Report the malaria status.
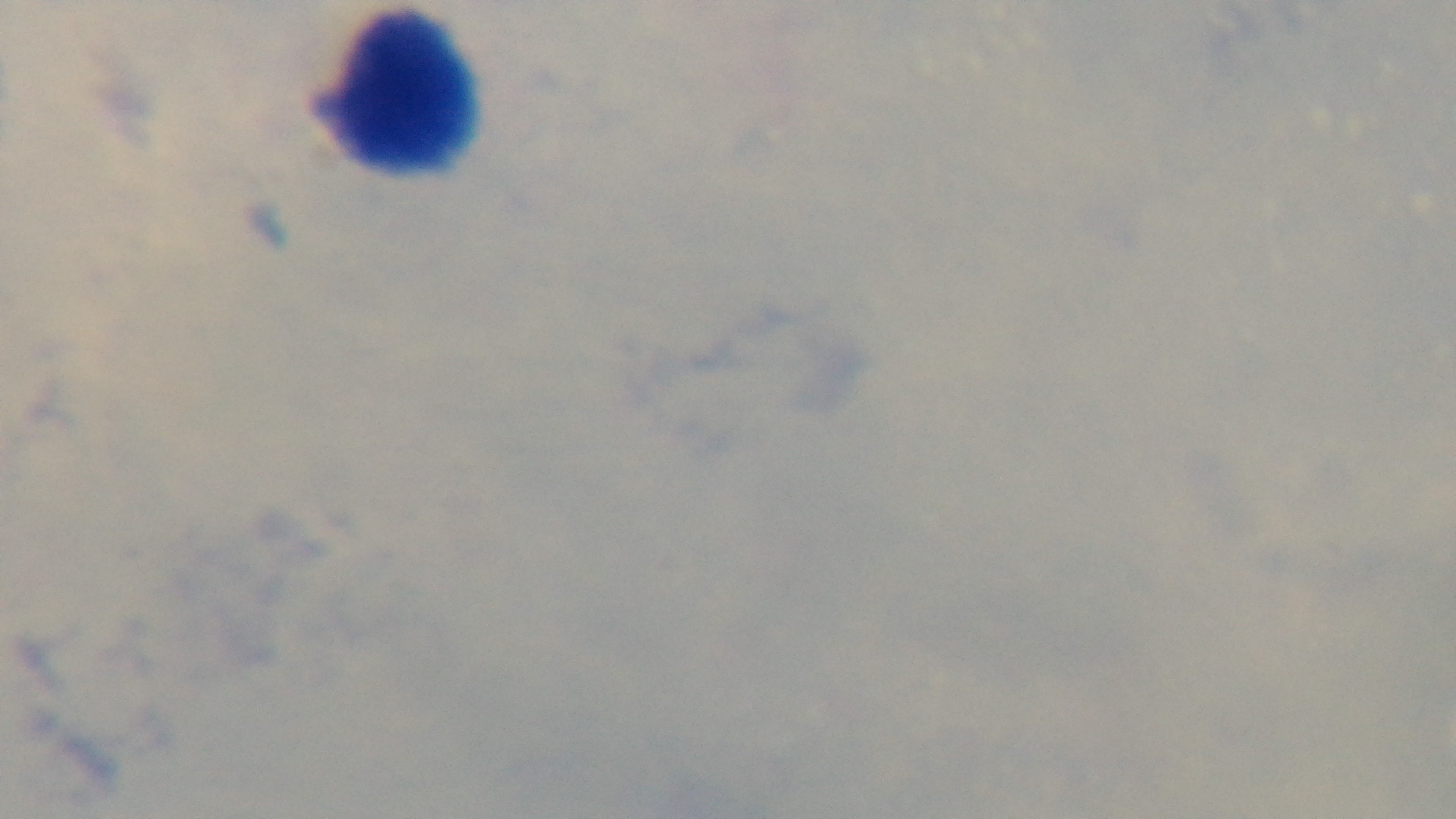
Negative.

One field from the slide. Giemsa stain. Mounted 4K digital camera. Oil-immersion objective, 100x. Photomicrograph. Preparation: thick blood film.